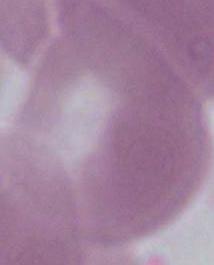
{
  "magnification": "1000x",
  "identification": "red blood cell",
  "modality": "micrograph"
}